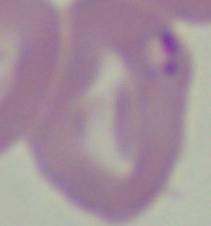

Summary:
  - Identification: Babesia
  - Magnification: 1000x
  - Modality: photomicrograph